Locate white blood cells.
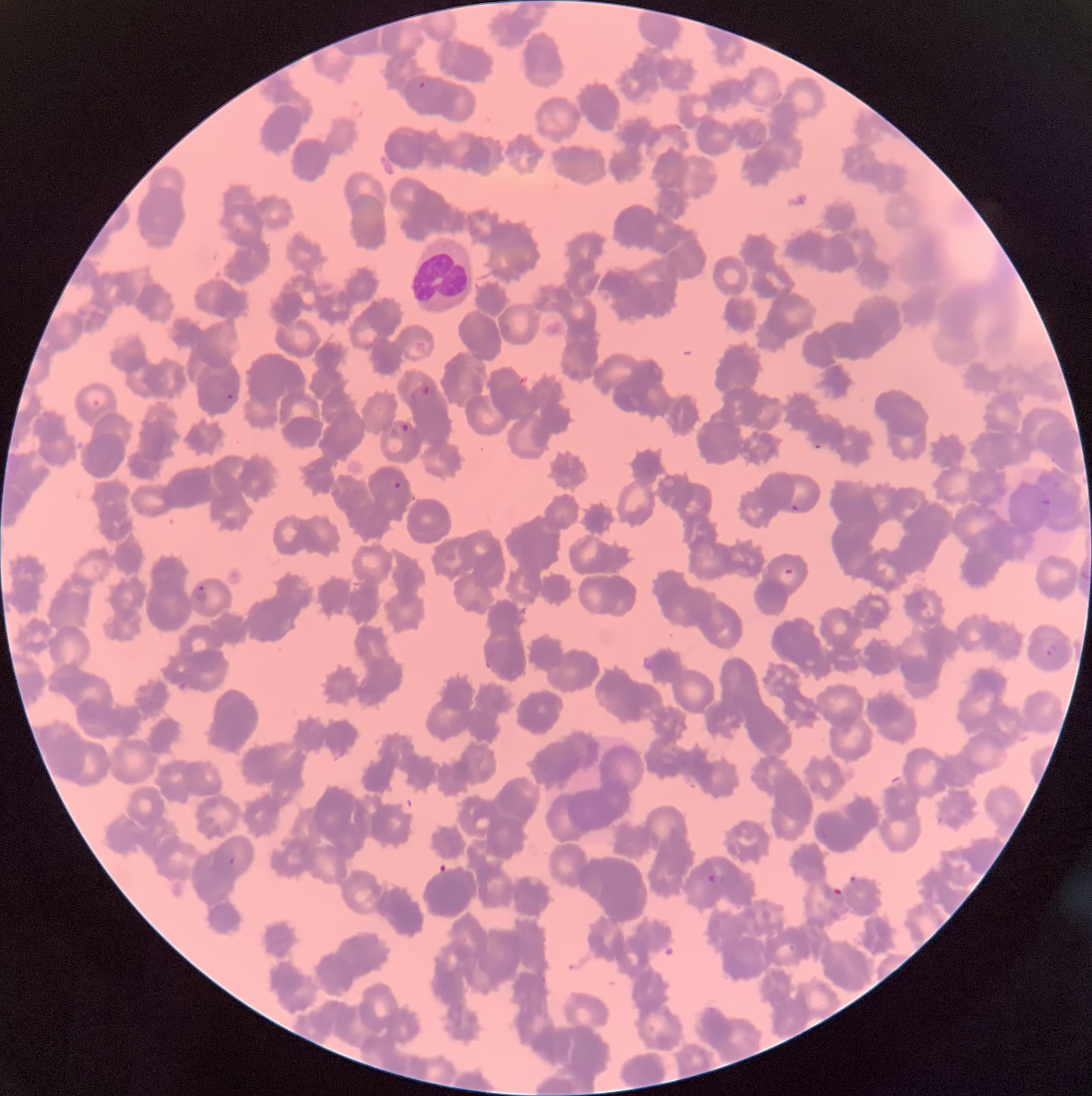
Approximate bounding boxes as [x1, y1, x2, y2] in pixels.
White blood cells: [412, 237, 472, 314].

Summary:
  - Plasmodium parasite locations: [417, 81, 427, 90], [757, 137, 766, 145], [409, 384, 435, 401], [224, 393, 235, 401], [401, 424, 410, 433], [812, 443, 822, 449], [391, 481, 403, 489], [1040, 499, 1053, 506], [790, 504, 801, 512], [779, 568, 799, 585], [1080, 570, 1089, 580], [192, 585, 208, 602], [1046, 644, 1058, 656], [485, 653, 494, 669], [223, 852, 237, 864], [708, 873, 726, 885], [848, 875, 861, 892]
  - Modality: light microscopy
  - Preparation: thin blood smear
  - Red blood cell morphology: rouleaux formation
  - Image size: 1092×1096 pixels